State which parasite is depicted.
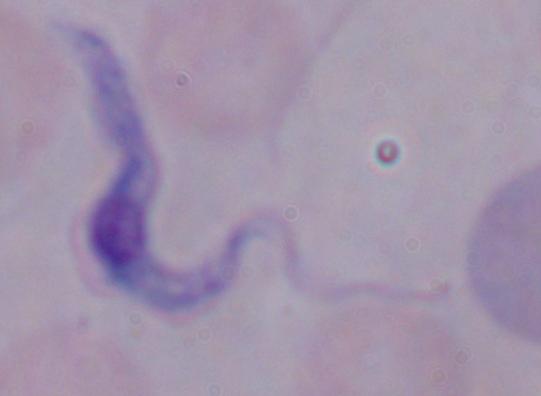
This is a trypanosome.

Summary:
  - Modality: micrograph
  - Magnification: 1000x